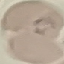

Result: malaria parasites identified. Thin blood film. Giemsa-stained preparation. Photographed with a smartphone camera at the microscope eyepiece. Cell patch, automatically extracted from a larger field of view and resized to 64 × 64 pixels.